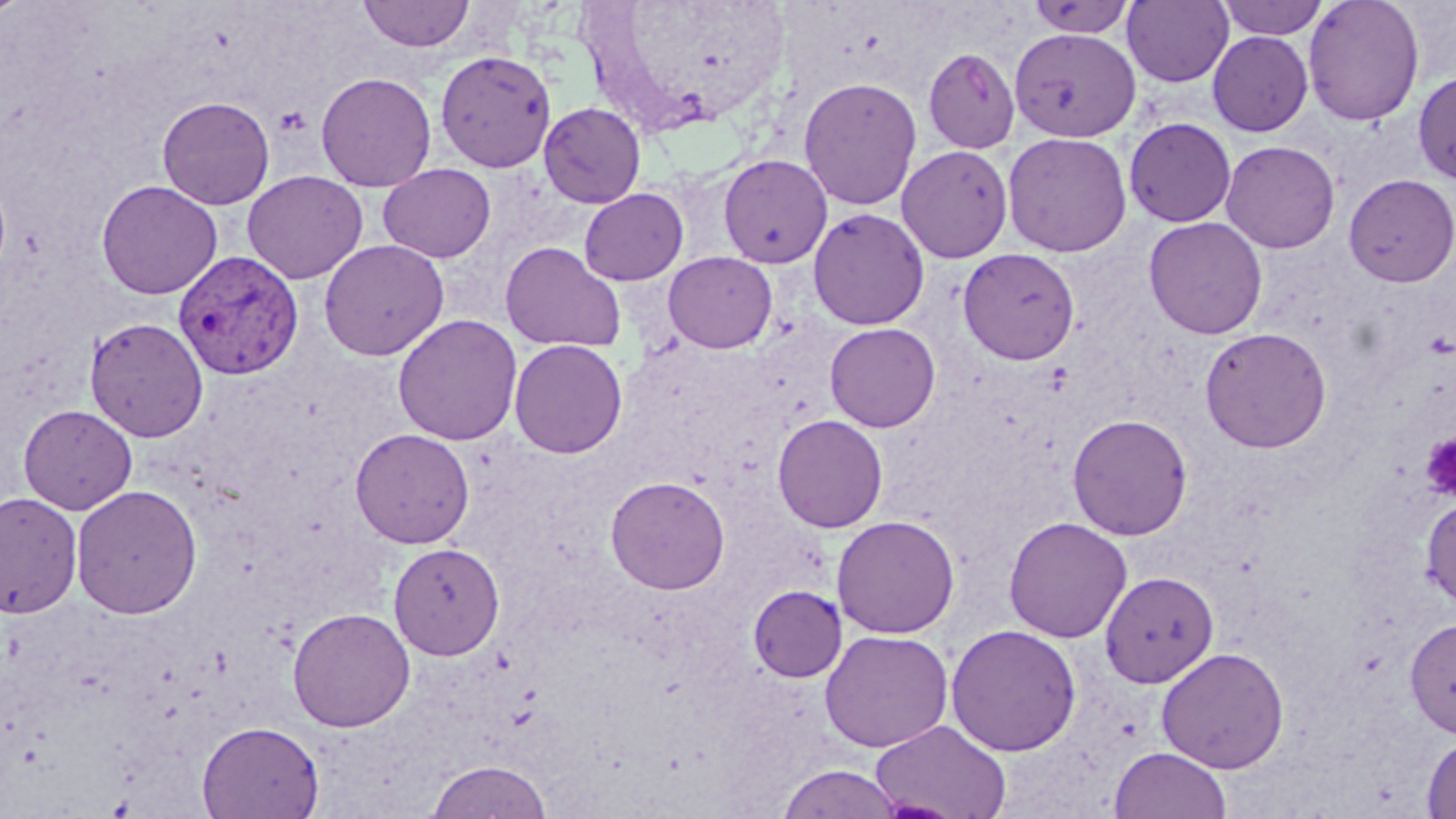

plasmodium_vivax_infected_red_blood_cell_locations: 'approximate bounding boxes as named x1/y1/x2/y2 corners in pixels: (x1=174, y1=249, x2=303, y2=380)'
slide_level_diagnosis: Plasmodium vivax
image_size: 1456×819 pixels
field_of_view: single
platelet_locations: 'approximate bounding boxes as named x1/y1/x2/y2 corners in pixels: (x1=273, y1=105, x2=312, y2=138), (x1=1421, y1=434, x2=1456, y2=500)'
preparation: thin blood film
modality: light microscopy
stain: May-Grünwald-Giemsa
uninfected_red_blood_cell_locations: 'approximate bounding boxes as named x1/y1/x2/y2 corners in pixels: (x1=0, y1=0, x2=31, y2=22), (x1=358, y1=0, x2=474, y2=51), (x1=1025, y1=0, x2=1137, y2=39), (x1=1122, y1=0, x2=1234, y2=87), (x1=1217, y1=0, x2=1330, y2=41), (x1=1303, y1=0, x2=1425, y2=127), (x1=1010, y1=28, x2=1140, y2=142), (x1=1207, y1=32, x2=1313, y2=136), (x1=923, y1=48, x2=1021, y2=153), (x1=435, y1=50, x2=557, y2=172), (x1=1413, y1=68, x2=1456, y2=185), (x1=316, y1=71, x2=437, y2=191), (x1=798, y1=77, x2=922, y2=211), (x1=157, y1=95, x2=275, y2=209), (x1=538, y1=102, x2=647, y2=208), (x1=1123, y1=117, x2=1236, y2=228), (x1=1002, y1=132, x2=1133, y2=257), (x1=1221, y1=140, x2=1340, y2=253), (x1=897, y1=145, x2=1013, y2=262), (x1=718, y1=154, x2=833, y2=268), (x1=377, y1=163, x2=496, y2=263), (x1=242, y1=170, x2=368, y2=284), (x1=1343, y1=173, x2=1456, y2=287), (x1=96, y1=179, x2=223, y2=299), (x1=579, y1=188, x2=689, y2=286), (x1=808, y1=208, x2=930, y2=330), (x1=1144, y1=216, x2=1268, y2=340), (x1=319, y1=239, x2=449, y2=360), (x1=500, y1=241, x2=626, y2=354), (x1=958, y1=247, x2=1080, y2=364), (x1=663, y1=252, x2=777, y2=353), (x1=392, y1=313, x2=523, y2=445), (x1=85, y1=316, x2=208, y2=442), (x1=825, y1=322, x2=940, y2=432), (x1=1200, y1=327, x2=1332, y2=453), (x1=509, y1=339, x2=628, y2=458), (x1=18, y1=404, x2=138, y2=514), (x1=1067, y1=413, x2=1193, y2=540), (x1=772, y1=414, x2=889, y2=532), (x1=350, y1=428, x2=475, y2=547), (x1=605, y1=475, x2=730, y2=595), (x1=71, y1=484, x2=202, y2=620), (x1=0, y1=492, x2=82, y2=619), (x1=1420, y1=496, x2=1456, y2=609), (x1=831, y1=515, x2=960, y2=638), (x1=1003, y1=516, x2=1133, y2=643), (x1=388, y1=542, x2=505, y2=660), (x1=1100, y1=571, x2=1218, y2=687), (x1=748, y1=584, x2=847, y2=682), (x1=287, y1=606, x2=416, y2=731), (x1=1405, y1=617, x2=1456, y2=739), (x1=945, y1=624, x2=1081, y2=756), (x1=819, y1=629, x2=953, y2=752), (x1=1155, y1=646, x2=1290, y2=773), (x1=871, y1=718, x2=1012, y2=819), (x1=197, y1=720, x2=324, y2=818), (x1=1421, y1=734, x2=1456, y2=818), (x1=1108, y1=746, x2=1233, y2=819), (x1=425, y1=759, x2=553, y2=819), (x1=776, y1=764, x2=904, y2=819)'
magnification: 1000x